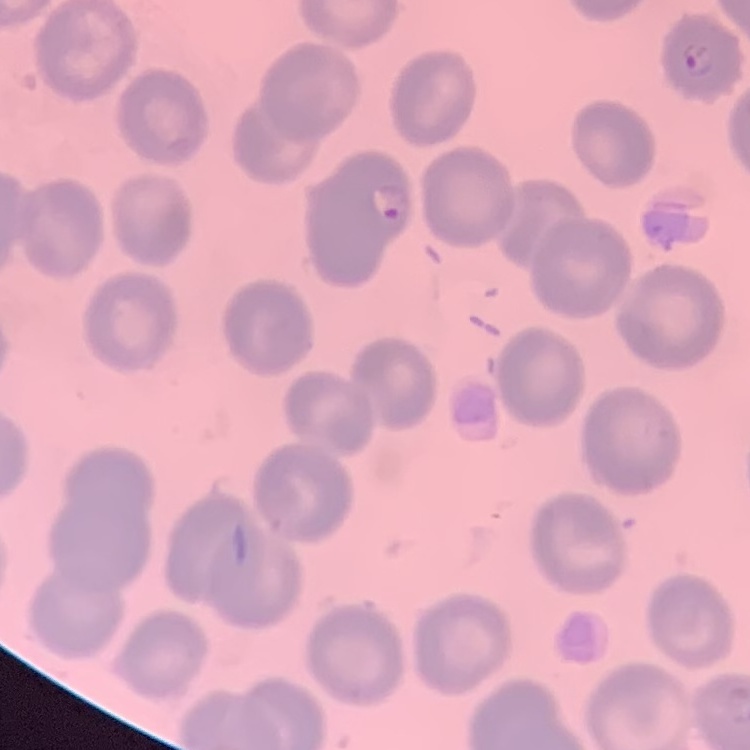

Summary:
  - Erythrocyte morphology: no rouleaux formation
  - Image type: one tile cut from a larger photomicrograph
  - Stain: Field's or Giemsa
  - Preparation: thin blood film